Locate every blood parasite and identify its species.
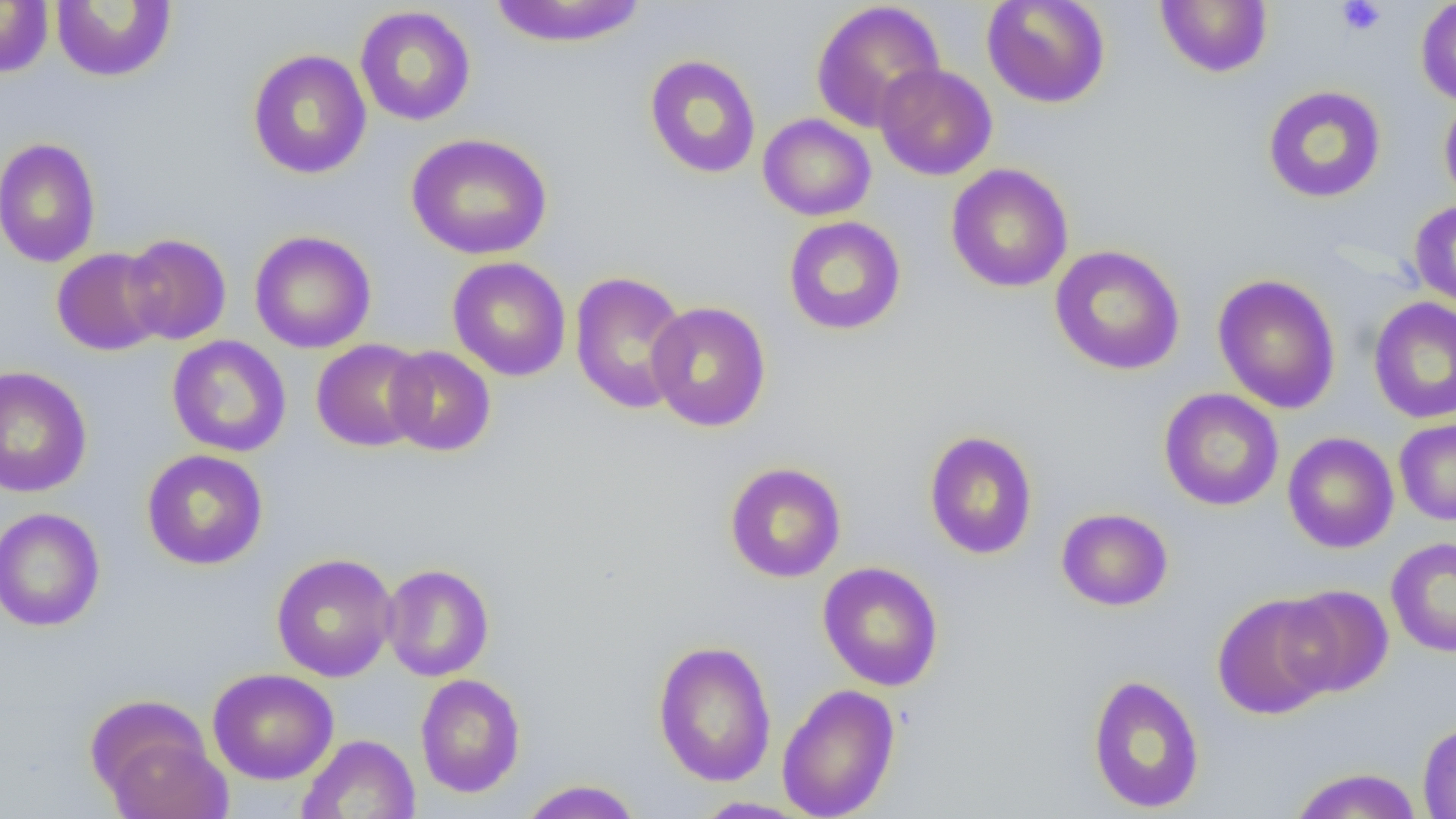
No blood parasites seen.

Summary:
  - Coordinate format: approximate bounding boxes as named x1/y1/x2/y2 corners in pixels
  - Uninfected red blood cell locations: (x1=981, y1=0, x2=1111, y2=109), (x1=1155, y1=0, x2=1273, y2=77), (x1=1415, y1=0, x2=1456, y2=107), (x1=0, y1=1, x2=54, y2=78), (x1=50, y1=1, x2=177, y2=83), (x1=488, y1=1, x2=648, y2=49), (x1=810, y1=1, x2=946, y2=132), (x1=354, y1=6, x2=476, y2=126), (x1=247, y1=49, x2=372, y2=179), (x1=644, y1=54, x2=761, y2=179), (x1=874, y1=62, x2=998, y2=181), (x1=1262, y1=85, x2=1387, y2=203), (x1=1439, y1=93, x2=1456, y2=212), (x1=758, y1=114, x2=876, y2=221), (x1=406, y1=132, x2=552, y2=260), (x1=0, y1=137, x2=101, y2=267), (x1=946, y1=163, x2=1073, y2=293), (x1=1408, y1=199, x2=1456, y2=312), (x1=783, y1=216, x2=906, y2=336), (x1=249, y1=230, x2=376, y2=354), (x1=121, y1=233, x2=232, y2=345), (x1=1049, y1=245, x2=1186, y2=375), (x1=51, y1=247, x2=167, y2=356), (x1=447, y1=256, x2=572, y2=381), (x1=569, y1=270, x2=692, y2=415), (x1=1212, y1=273, x2=1341, y2=413), (x1=1368, y1=295, x2=1456, y2=425), (x1=647, y1=301, x2=772, y2=432), (x1=166, y1=335, x2=292, y2=458), (x1=311, y1=339, x2=430, y2=452), (x1=384, y1=346, x2=496, y2=457), (x1=0, y1=365, x2=92, y2=498), (x1=1158, y1=388, x2=1284, y2=511), (x1=1394, y1=418, x2=1456, y2=526), (x1=923, y1=430, x2=1038, y2=559), (x1=1282, y1=432, x2=1399, y2=553), (x1=141, y1=449, x2=268, y2=570), (x1=724, y1=462, x2=846, y2=582), (x1=0, y1=507, x2=105, y2=632), (x1=1056, y1=507, x2=1173, y2=611), (x1=1386, y1=536, x2=1456, y2=657), (x1=271, y1=552, x2=398, y2=682), (x1=817, y1=561, x2=944, y2=692), (x1=381, y1=563, x2=494, y2=681), (x1=1278, y1=584, x2=1393, y2=697), (x1=1212, y1=593, x2=1340, y2=719), (x1=653, y1=640, x2=777, y2=787), (x1=208, y1=667, x2=338, y2=785), (x1=414, y1=673, x2=526, y2=798), (x1=1086, y1=673, x2=1206, y2=814), (x1=777, y1=683, x2=901, y2=819), (x1=96, y1=721, x2=232, y2=819), (x1=1417, y1=721, x2=1456, y2=818), (x1=297, y1=734, x2=421, y2=819), (x1=1289, y1=767, x2=1423, y2=819), (x1=518, y1=779, x2=644, y2=818), (x1=691, y1=796, x2=812, y2=818)
  - Platelet locations: (x1=1336, y1=0, x2=1386, y2=36)
  - Slide-level diagnosis: no evidence of blood parasites
  - Modality: optical microscopy
  - Preparation: thin blood smear
  - Image size: 1456×819 pixels
  - Field of view: one of a larger specimen
  - Magnification: 1000x